Assess this cell for malaria.
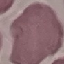

It is uninfected.

Summary:
  - Stain: Giemsa
  - Image type: automatically extracted cell patch, resized to 64 × 64 pixels
  - Preparation: thin blood smear
  - Capture: smartphone camera at the microscope eyepiece